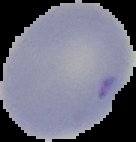
Summary:
  - Image size: 136×142 pixels
  - Result: no malaria parasites seen
  - Preparation: thin blood smear
  - Image type: cell region segmented out of the field of view; surrounding area masked to black